Locate every blood parasite and identify its species.
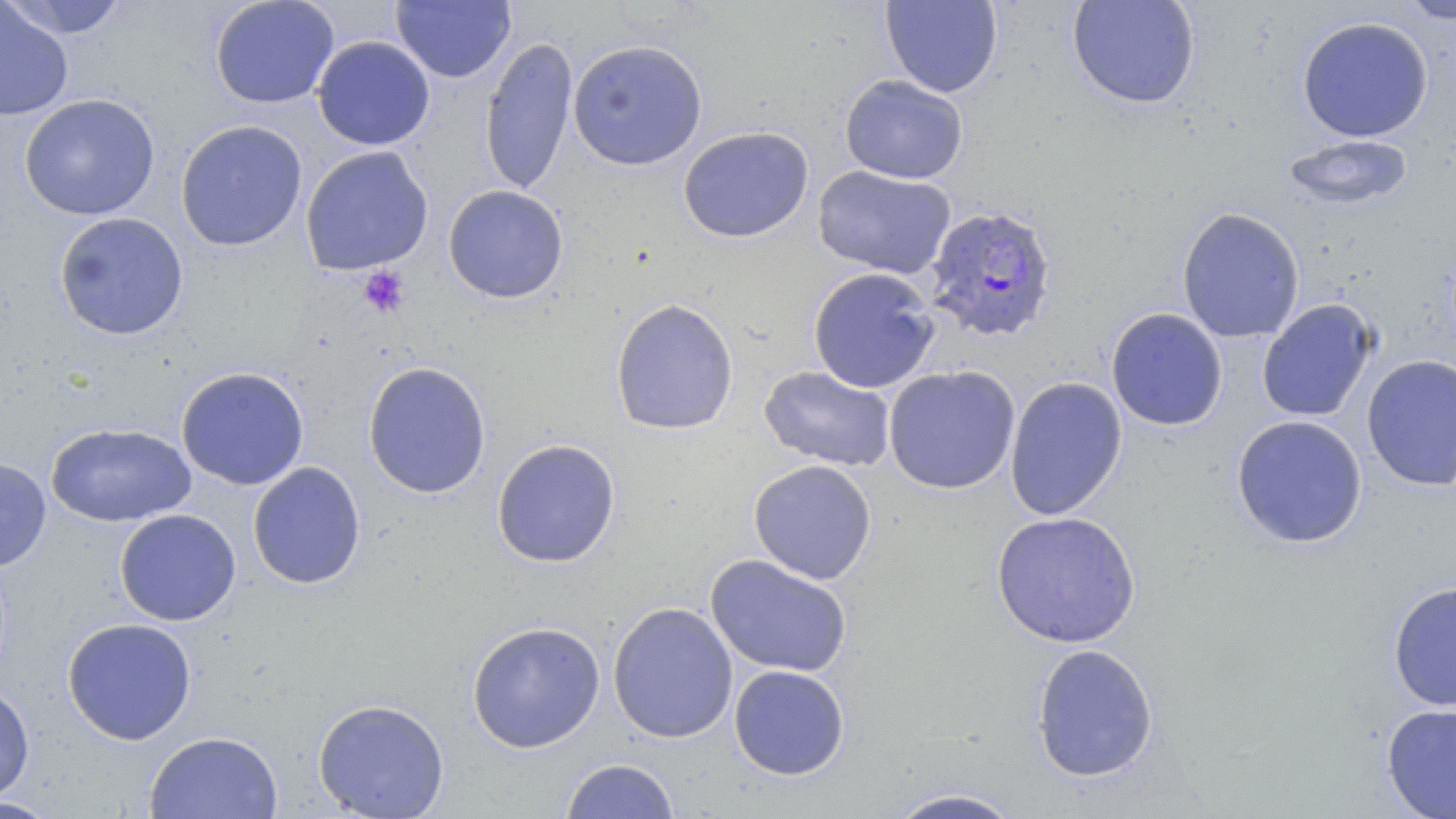

Approximate bounding boxes as [x1, y1, x2, y2] in pixels.
Plasmodium falciparum-infected red blood cells: [923, 204, 1058, 343].
No Plasmodium ovale, Plasmodium malariae, Plasmodium vivax, Babesia divergens, or Trypanosoma brucei observed.

slide-level diagnosis = Plasmodium falciparum
field of view = single
magnification = 1000x
preparation = thin blood smear
platelet locations = approximate bounding boxes as [x1, y1, x2, y2] in pixels: [357, 266, 410, 318]
modality = light microscopy
image size = 1456×819 pixels
stain = May-Grünwald-Giemsa
uninfected red blood cell locations = approximate bounding boxes as [x1, y1, x2, y2] in pixels: [3, 0, 130, 40], [209, 0, 340, 109], [880, 0, 1003, 98], [1066, 0, 1201, 109], [1396, 0, 1456, 24], [391, 1, 515, 84], [0, 2, 74, 121], [1296, 16, 1434, 143], [312, 35, 435, 151], [480, 35, 578, 196], [567, 39, 708, 170], [839, 74, 969, 185], [19, 93, 160, 221], [175, 119, 307, 252], [678, 125, 814, 243], [1282, 135, 1413, 210], [300, 145, 433, 276], [813, 165, 957, 280], [443, 185, 569, 304], [1176, 206, 1305, 344], [53, 212, 189, 340], [807, 266, 940, 394], [609, 297, 740, 436], [1256, 298, 1379, 423], [1105, 308, 1228, 432], [1362, 354, 1456, 491], [362, 360, 491, 499], [758, 365, 896, 472], [883, 365, 1021, 494], [175, 366, 309, 491], [1004, 376, 1128, 521], [1231, 414, 1368, 549], [47, 423, 196, 527], [491, 438, 621, 567], [0, 458, 51, 571], [748, 459, 878, 584], [247, 461, 366, 589], [114, 508, 241, 626], [990, 510, 1142, 649], [705, 553, 853, 678], [1387, 579, 1456, 712], [607, 600, 738, 743], [62, 617, 197, 745], [466, 620, 605, 753], [1030, 642, 1159, 783], [729, 664, 850, 780], [0, 681, 35, 804], [312, 698, 450, 819], [1380, 701, 1456, 819], [144, 730, 283, 819], [559, 758, 681, 818], [884, 787, 1025, 819], [0, 795, 64, 819]